Point out each leukocyte.
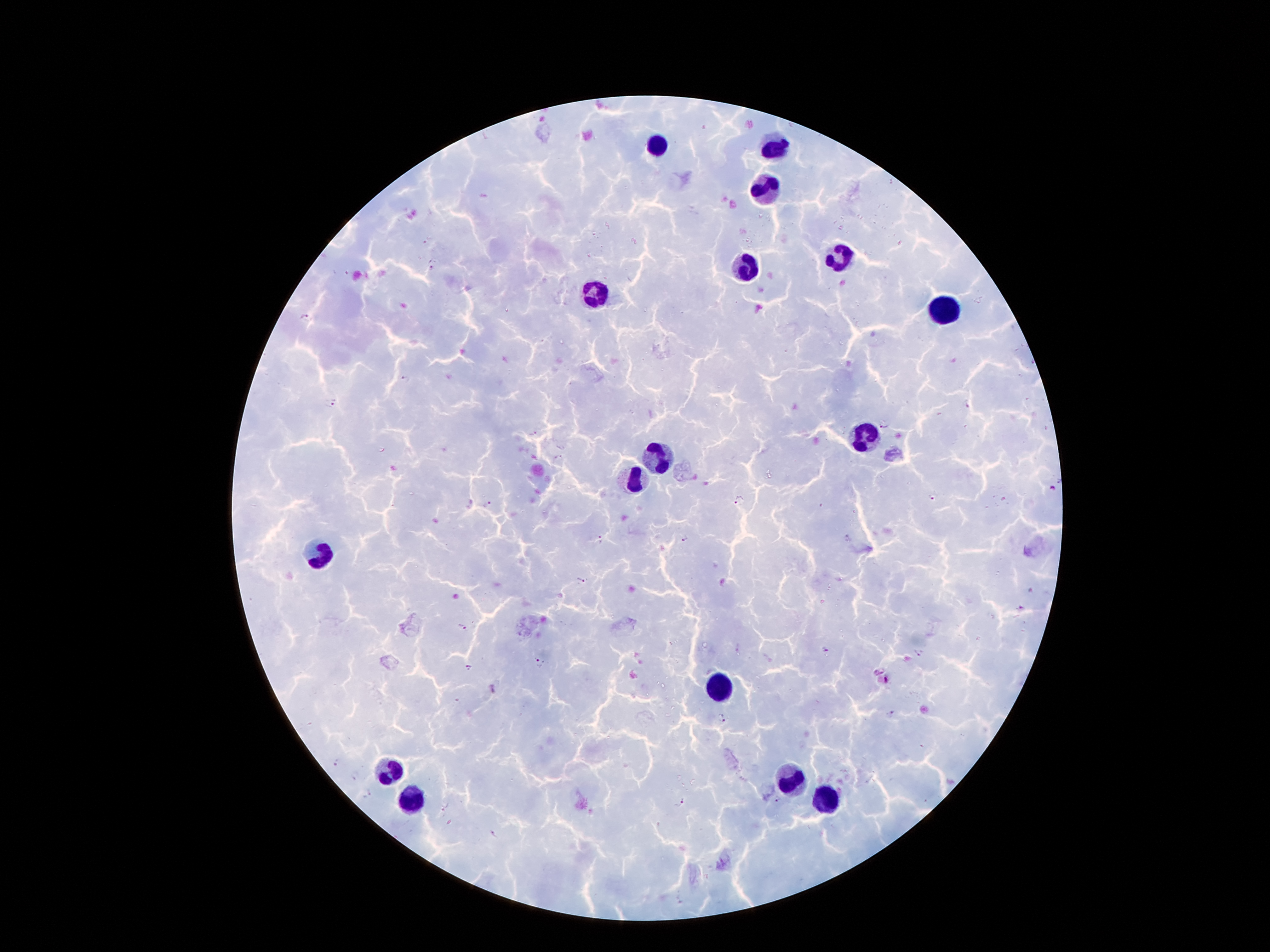
Approximate centers as {x, y} in pixels.
Leukocytes: {658, 142}, {773, 147}, {762, 186}, {837, 255}, {749, 266}, {598, 295}, {941, 310}, {861, 434}, {660, 456}, {634, 478}, {318, 555}, {718, 683}, {388, 767}, {788, 778}, {410, 798}, {824, 801}.

Malaria parasite locations: {426, 240}, {434, 269}, {307, 318}, {404, 377}, {333, 403}, {966, 405}, {882, 424}, {533, 435}, {558, 458}, {1053, 488}, {935, 496}, {739, 499}, {487, 503}, {686, 538}, {600, 540}, {580, 580}, {461, 626}, {825, 649}, {918, 652}, {540, 663}, {467, 667}, {891, 714}, {722, 718}, {338, 765}, {355, 775}, {369, 794}, {682, 802}. Thick blood film. Single field of view. Patient malaria status: infected with Plasmodium falciparum. Image is 1270×952 pixels. 100x magnification. Smartphone photograph taken through the microscope eyepiece. Giemsa-stained preparation.